Locate and identify every blood parasite.
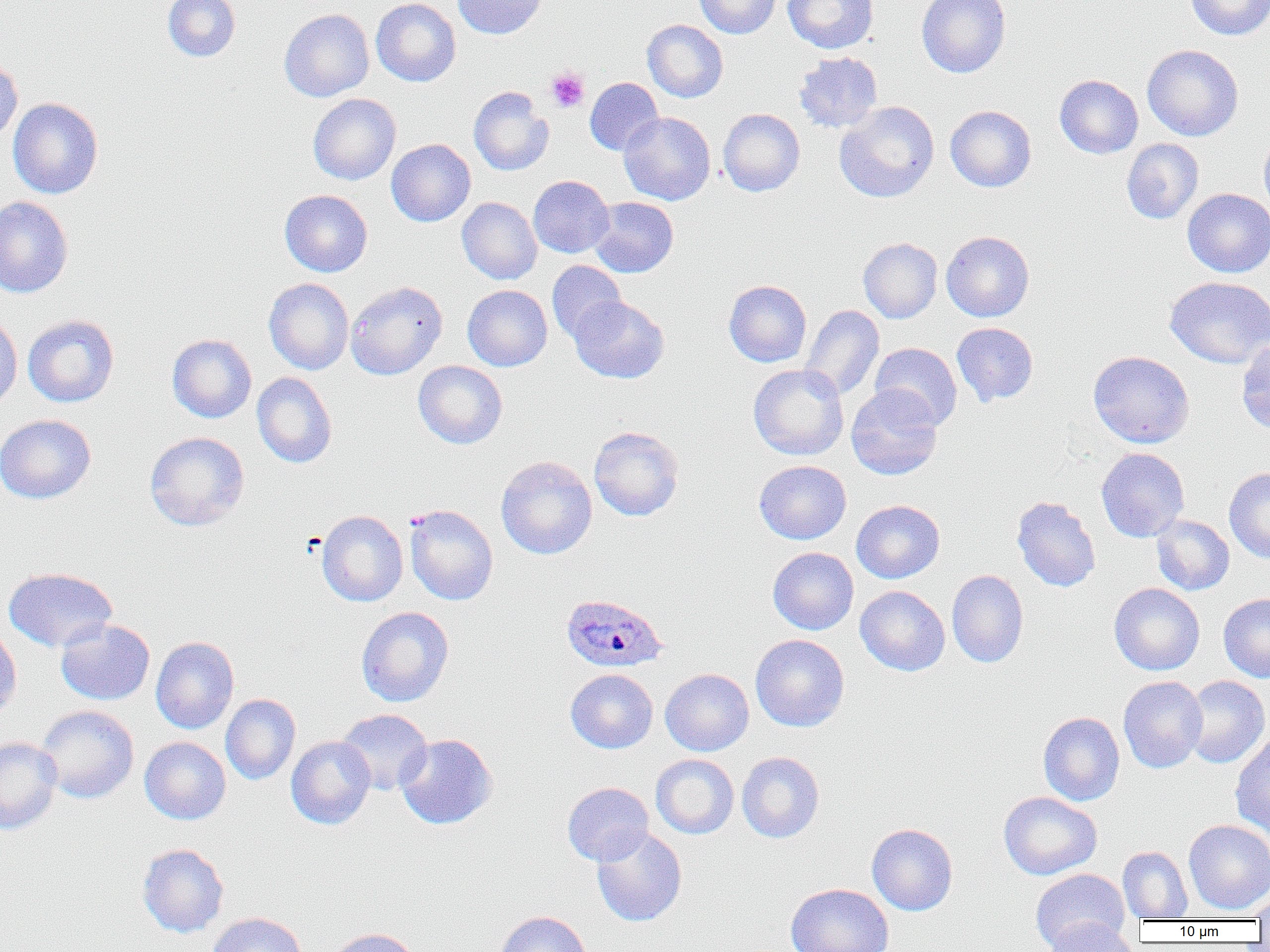
Approximate bounding boxes as named x1/y1/x2/y2 corners in pixels.
Plasmodium ovale-infected red blood cells: (x1=560, y1=593, x2=668, y2=673).
No Plasmodium falciparum, Plasmodium malariae, Plasmodium vivax, Babesia divergens, or Trypanosoma brucei observed.

Uninfected red blood cell locations: (x1=162, y1=0, x2=241, y2=62), (x1=370, y1=0, x2=461, y2=87), (x1=453, y1=0, x2=547, y2=39), (x1=694, y1=0, x2=781, y2=38), (x1=782, y1=0, x2=878, y2=54), (x1=916, y1=0, x2=1011, y2=78), (x1=1184, y1=0, x2=1270, y2=41), (x1=279, y1=8, x2=374, y2=102), (x1=642, y1=20, x2=728, y2=102), (x1=1142, y1=44, x2=1243, y2=141), (x1=794, y1=51, x2=883, y2=133), (x1=0, y1=53, x2=23, y2=146), (x1=1054, y1=74, x2=1143, y2=159), (x1=585, y1=77, x2=663, y2=156), (x1=468, y1=86, x2=554, y2=176), (x1=308, y1=93, x2=401, y2=185), (x1=7, y1=97, x2=103, y2=199), (x1=834, y1=101, x2=939, y2=203), (x1=945, y1=105, x2=1036, y2=192), (x1=718, y1=108, x2=805, y2=196), (x1=619, y1=111, x2=715, y2=205), (x1=1259, y1=132, x2=1270, y2=222), (x1=1121, y1=138, x2=1204, y2=224), (x1=386, y1=139, x2=475, y2=227), (x1=528, y1=175, x2=614, y2=258), (x1=1183, y1=188, x2=1270, y2=278), (x1=280, y1=189, x2=373, y2=277), (x1=0, y1=195, x2=74, y2=299), (x1=589, y1=196, x2=679, y2=277), (x1=457, y1=197, x2=542, y2=284), (x1=941, y1=230, x2=1035, y2=322), (x1=858, y1=237, x2=942, y2=323), (x1=546, y1=261, x2=626, y2=343), (x1=1165, y1=276, x2=1270, y2=369), (x1=264, y1=278, x2=354, y2=375), (x1=345, y1=280, x2=447, y2=379), (x1=724, y1=280, x2=812, y2=367), (x1=463, y1=285, x2=552, y2=371), (x1=570, y1=295, x2=669, y2=383), (x1=800, y1=305, x2=884, y2=400), (x1=0, y1=314, x2=23, y2=411), (x1=22, y1=314, x2=119, y2=407), (x1=951, y1=322, x2=1039, y2=407), (x1=167, y1=334, x2=257, y2=423), (x1=1236, y1=339, x2=1270, y2=435), (x1=869, y1=342, x2=962, y2=430), (x1=1088, y1=350, x2=1195, y2=448), (x1=413, y1=360, x2=507, y2=449), (x1=748, y1=364, x2=848, y2=460), (x1=252, y1=372, x2=337, y2=468), (x1=846, y1=385, x2=943, y2=480), (x1=0, y1=414, x2=96, y2=504), (x1=589, y1=426, x2=684, y2=521), (x1=144, y1=431, x2=250, y2=531), (x1=1096, y1=448, x2=1190, y2=542), (x1=496, y1=455, x2=597, y2=559), (x1=754, y1=460, x2=851, y2=544), (x1=1224, y1=468, x2=1270, y2=563), (x1=1011, y1=496, x2=1101, y2=592), (x1=851, y1=500, x2=945, y2=583), (x1=405, y1=504, x2=498, y2=605), (x1=316, y1=510, x2=408, y2=607), (x1=1151, y1=515, x2=1234, y2=595), (x1=768, y1=547, x2=858, y2=635), (x1=3, y1=567, x2=118, y2=653), (x1=947, y1=569, x2=1028, y2=668), (x1=1109, y1=583, x2=1205, y2=675), (x1=855, y1=585, x2=950, y2=676), (x1=1218, y1=593, x2=1270, y2=682), (x1=356, y1=606, x2=454, y2=707), (x1=56, y1=619, x2=155, y2=705), (x1=0, y1=625, x2=22, y2=720), (x1=750, y1=634, x2=849, y2=732), (x1=151, y1=636, x2=239, y2=734), (x1=565, y1=668, x2=658, y2=753), (x1=660, y1=668, x2=754, y2=756), (x1=1118, y1=675, x2=1208, y2=773), (x1=1182, y1=675, x2=1269, y2=768), (x1=221, y1=693, x2=301, y2=785), (x1=36, y1=705, x2=139, y2=804), (x1=336, y1=708, x2=433, y2=795), (x1=1038, y1=712, x2=1125, y2=805), (x1=1231, y1=733, x2=1270, y2=837), (x1=395, y1=734, x2=497, y2=829), (x1=286, y1=736, x2=376, y2=829), (x1=0, y1=737, x2=62, y2=835), (x1=139, y1=737, x2=231, y2=825), (x1=736, y1=751, x2=824, y2=843), (x1=650, y1=754, x2=739, y2=839), (x1=562, y1=782, x2=654, y2=867), (x1=998, y1=791, x2=1102, y2=880), (x1=1184, y1=819, x2=1270, y2=913), (x1=867, y1=823, x2=958, y2=916), (x1=591, y1=827, x2=687, y2=927), (x1=137, y1=843, x2=229, y2=938), (x1=1118, y1=845, x2=1193, y2=921), (x1=1030, y1=868, x2=1131, y2=951), (x1=785, y1=883, x2=894, y2=952), (x1=1250, y1=889, x2=1270, y2=925), (x1=495, y1=911, x2=592, y2=952), (x1=206, y1=912, x2=307, y2=952), (x1=1045, y1=917, x2=1136, y2=952), (x1=326, y1=927, x2=422, y2=952). Platelet locations: (x1=546, y1=67, x2=590, y2=112). Slide-level diagnosis: Plasmodium ovale. One field of a larger specimen. Optical microscopy. Captured at 1000x magnification. Image is 1270×952 pixels. Thin blood smear.